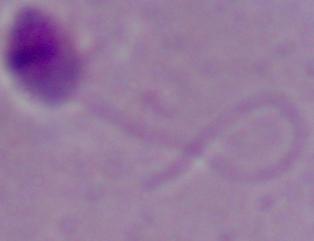

magnification = 1000x
identification = Leishmania
modality = micrograph